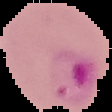
Result: malaria parasites detected. Image is 112×112 pixels. Cell region segmented out of the field of view; the surrounding area is masked to black. From a thin blood smear.